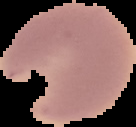

preparation = thin blood film
image type = segmented cell region with the area outside set to black
malaria status = parasitized
image size = 136×127 pixels